Assess this cell for malaria.
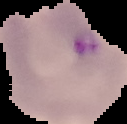
It is parasitized.

Summary:
  - Image size: 127×124 pixels
  - Image type: cell region segmented out of the field of view; surrounding area masked to black
  - Preparation: thin blood film